Locate platelets.
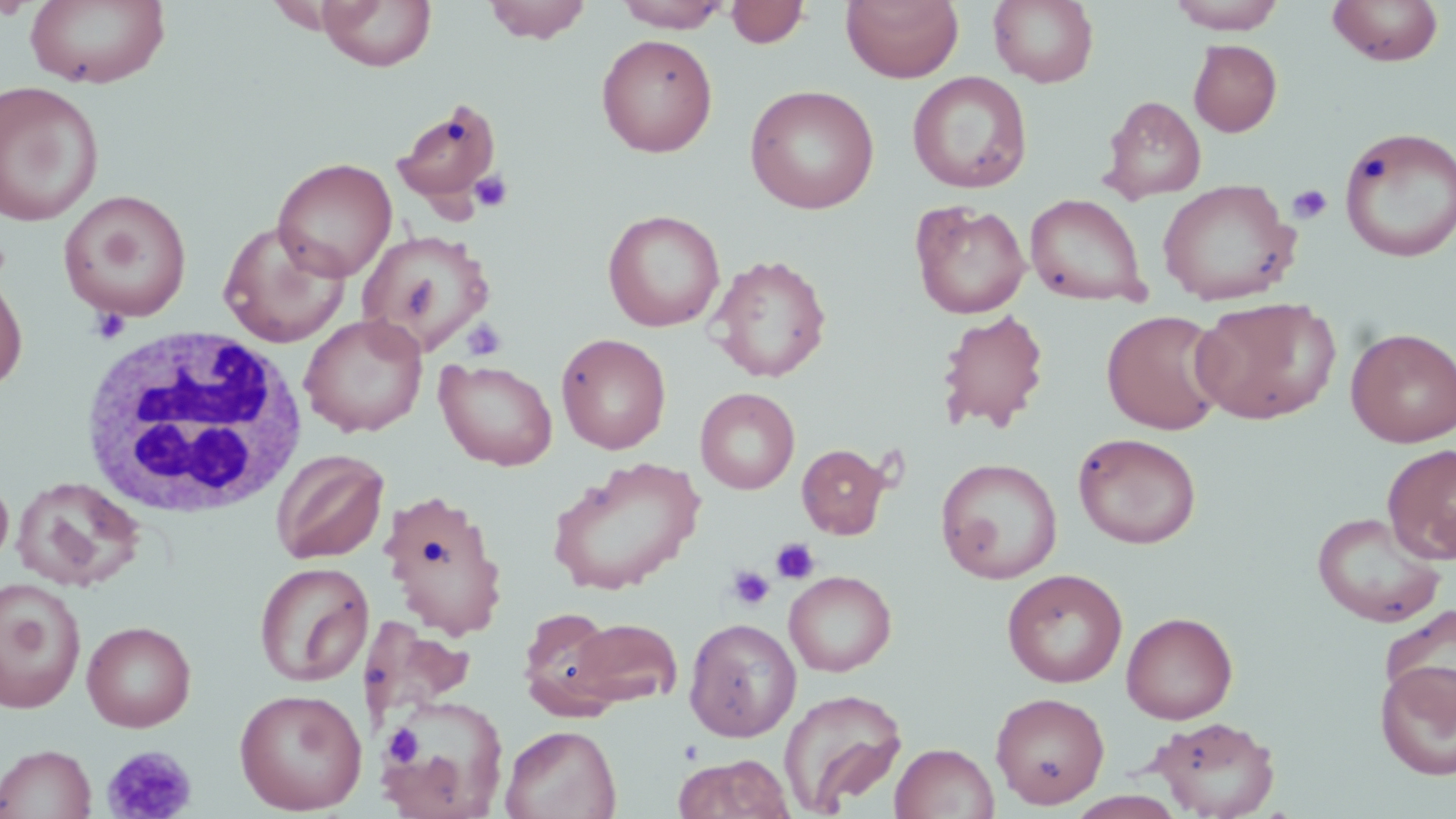
Approximate bounding boxes as [x1, y1, x2, y2] in pixels.
Platelets: [469, 169, 514, 214], [1287, 184, 1333, 224], [89, 308, 130, 344], [461, 318, 507, 360], [771, 538, 820, 585], [726, 566, 774, 610], [383, 724, 421, 767], [101, 744, 197, 819].

White blood cell locations: [79, 325, 309, 523]. Uninfected red blood cell locations: [25, 0, 171, 89], [317, 0, 437, 71], [483, 0, 593, 44], [841, 0, 964, 84], [988, 0, 1099, 88], [1168, 0, 1287, 33], [1327, 0, 1444, 66], [615, 1, 731, 32], [726, 1, 809, 48], [596, 33, 718, 157], [1188, 39, 1282, 137], [907, 71, 1033, 194], [0, 81, 105, 226], [744, 84, 880, 214], [1101, 95, 1206, 203], [392, 100, 502, 207], [1338, 126, 1456, 263], [272, 157, 397, 282], [1158, 179, 1301, 306], [58, 189, 193, 322], [1025, 193, 1149, 306], [910, 200, 1031, 319], [603, 210, 725, 332], [218, 221, 350, 347], [357, 229, 496, 355], [709, 254, 832, 383], [0, 265, 29, 395], [1190, 296, 1341, 425], [935, 308, 1050, 434], [1100, 309, 1229, 435], [300, 314, 428, 437], [1346, 327, 1456, 447], [556, 333, 671, 454], [435, 359, 558, 471], [695, 387, 800, 494], [1072, 432, 1201, 549], [797, 443, 891, 539], [1382, 444, 1456, 564], [271, 449, 389, 564], [547, 456, 704, 595], [936, 457, 1063, 583], [0, 474, 14, 573], [11, 476, 144, 592], [379, 489, 509, 642], [1311, 511, 1447, 628], [254, 561, 374, 687], [1002, 568, 1127, 688], [784, 570, 897, 677], [0, 579, 87, 713], [1380, 603, 1455, 718], [518, 607, 625, 718], [1121, 611, 1238, 724], [564, 617, 683, 709], [684, 617, 801, 742], [356, 618, 489, 720], [81, 620, 196, 732], [1374, 660, 1456, 781], [234, 687, 368, 814], [779, 688, 908, 814], [990, 691, 1110, 809], [377, 694, 509, 818], [1152, 716, 1281, 818], [501, 724, 621, 819], [890, 743, 999, 819], [0, 744, 96, 818], [673, 754, 795, 819]. Slide-level diagnosis: no evidence of blood parasites. Thin blood film. One field of a larger specimen. May-Grünwald-Giemsa stain. Light microscopy. 1000x magnification. Image is 1456×819 pixels.